Name the blood parasite species.
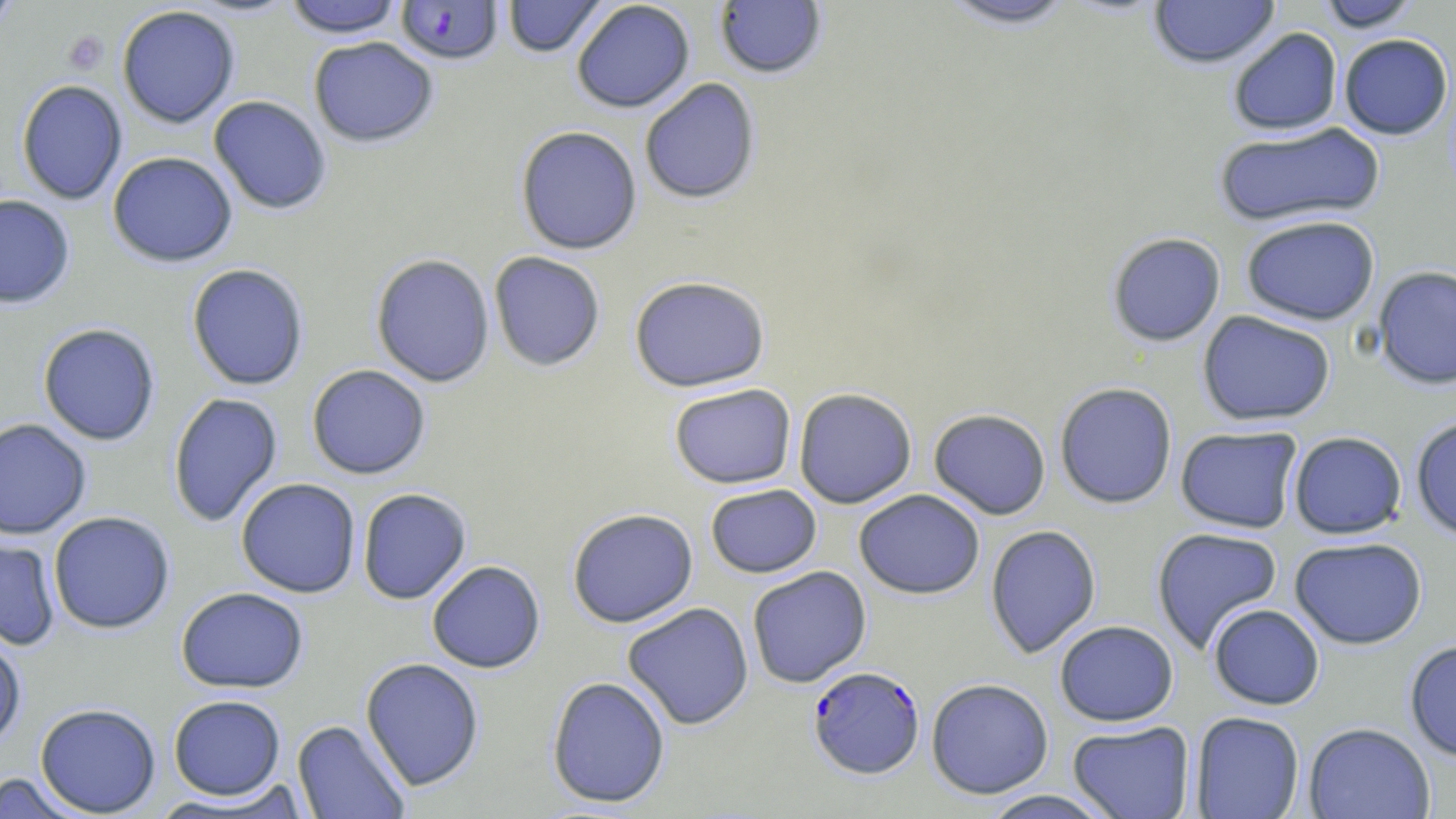

Plasmodium falciparum.

Approximate bounding boxes as [x1, y1, x2, y2] in pixels. Uninfected red blood cell locations: [0, 0, 24, 33], [284, 0, 403, 38], [502, 0, 608, 58], [936, 0, 1079, 30], [1148, 0, 1281, 69], [1317, 0, 1420, 32], [571, 1, 695, 113], [714, 1, 828, 80], [116, 4, 240, 129], [1227, 27, 1343, 136], [1338, 33, 1453, 140], [308, 36, 439, 147], [639, 77, 761, 205], [15, 79, 128, 205], [208, 95, 332, 215], [1213, 121, 1385, 228], [515, 125, 643, 255], [107, 151, 238, 267], [0, 194, 75, 308], [1240, 214, 1380, 326], [1106, 231, 1226, 346], [488, 251, 606, 372], [370, 253, 495, 387], [186, 263, 309, 391], [1372, 265, 1456, 390], [628, 274, 771, 392], [1197, 310, 1336, 426], [37, 323, 161, 446], [306, 364, 432, 480], [1054, 382, 1178, 509], [668, 383, 797, 489], [793, 387, 918, 508], [167, 393, 284, 528], [928, 408, 1051, 519], [1410, 416, 1456, 541], [0, 418, 92, 540], [1175, 425, 1303, 534], [1288, 431, 1407, 539], [235, 478, 361, 598], [705, 484, 822, 578], [357, 488, 472, 604], [853, 489, 985, 599], [566, 508, 698, 628], [48, 511, 175, 634], [985, 524, 1102, 659], [1151, 526, 1284, 654], [0, 534, 61, 651], [1289, 536, 1428, 649], [426, 560, 546, 673], [746, 566, 872, 688], [175, 587, 309, 693], [622, 602, 754, 730], [1208, 604, 1325, 710], [1054, 620, 1179, 726], [0, 628, 27, 750], [1404, 639, 1456, 762], [360, 657, 485, 791], [546, 676, 671, 808], [925, 678, 1054, 799], [168, 694, 285, 800], [35, 702, 161, 816], [1189, 711, 1305, 818], [292, 719, 411, 818], [1067, 720, 1196, 819], [1303, 722, 1435, 819], [0, 771, 86, 818], [148, 785, 311, 816], [978, 789, 1119, 818]. Plasmodium falciparum-infected red blood cell locations: [394, 1, 504, 66], [808, 665, 925, 779]. Platelet locations: [63, 31, 108, 74]. Captured at 1000x magnification. May-Grünwald-Giemsa-stained preparation. Image is 1456×819 pixels. Single field of view. Optical microscopy. Thin blood film.